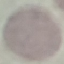

Malaria status: uninfected. Thin blood smear. Giemsa stain. Automatically extracted cell patch, resized to 64 × 64 pixels. Photographed with a smartphone camera at the microscope eyepiece.